Assess this cell for malaria.
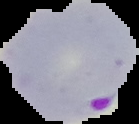

Parasitized.

preparation = thin blood film
image type = cell region segmented out of the field of view; surrounding area masked to black
image size = 139×124 pixels